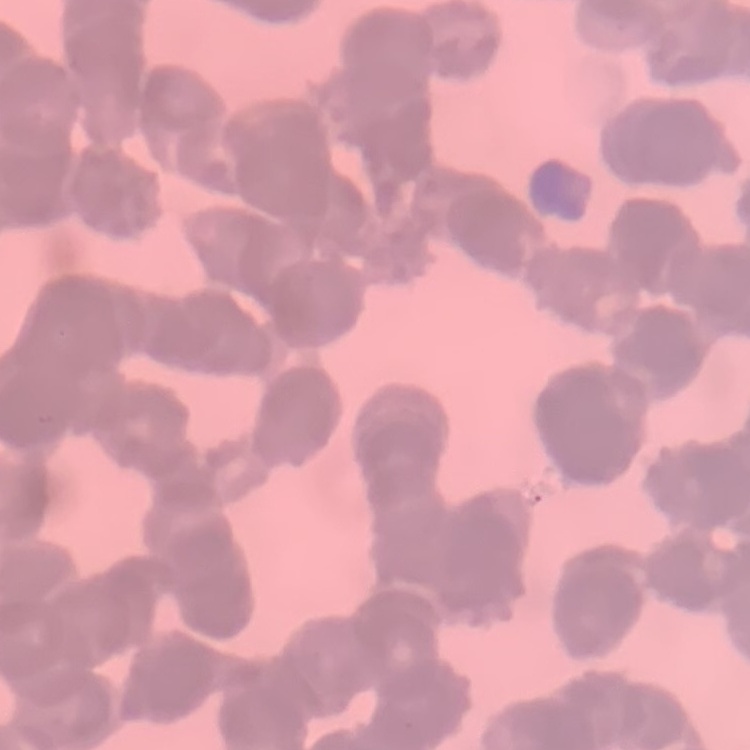
The erythrocytes show rouleaux formation. Stained with either Field's or Giemsa. One tile cut from a larger photomicrograph. Thin blood smear.